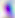

Summary:
  - Identification: Toxoplasma gondii
  - Modality: micrograph
  - Magnification: 400x